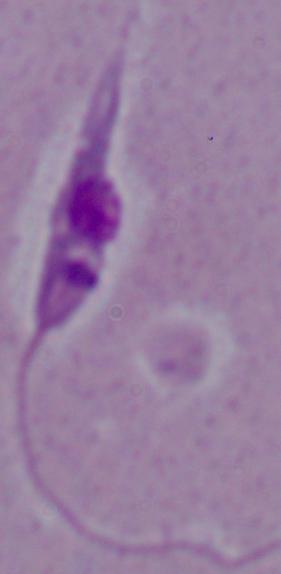
{
  "identification": "Leishmania",
  "modality": "photomicrograph",
  "magnification": "1000x"
}